Classify this cell by malaria status.
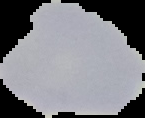

It is uninfected.

image type = cell region segmented out of the field of view; surrounding area masked to black
image size = 145×118 pixels
preparation = thin blood smear